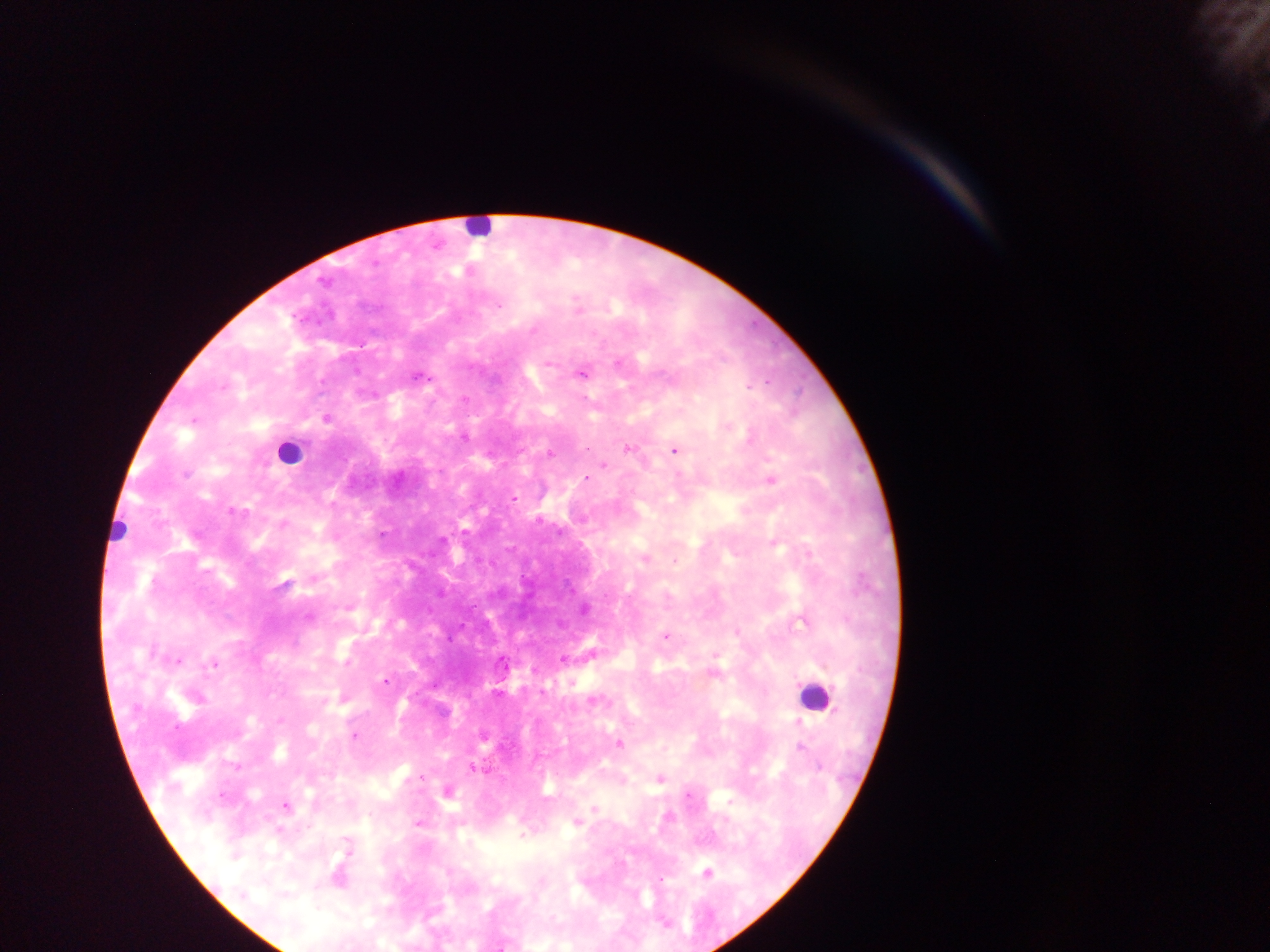

Plasmodium parasite locations = approximate centers as (x, y) in pixels: (498, 307), (533, 330), (549, 363), (580, 373), (418, 376), (767, 381), (755, 385), (464, 399), (326, 419), (463, 436), (628, 447), (587, 448), (674, 450), (549, 454), (605, 465), (187, 474), (585, 478), (513, 498), (244, 510), (231, 511), (540, 520), (466, 529), (442, 539), (674, 562), (665, 637), (177, 661), (214, 664), (385, 680), (353, 736), (472, 768), (424, 777), (223, 796), (285, 806), (418, 821), (661, 878)
leukocyte locations = approximate centers as (x, y) in pixels: (482, 226), (288, 456), (811, 698)
capture = mobile-phone photograph through a microscope
image size = 1270×952 pixels
preparation = thick blood smear
field of view = single
country = Ghana